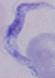
magnification = 1000x
identification = trypanosome
modality = photomicrograph